Comment on the morphology of the erythrocytes.
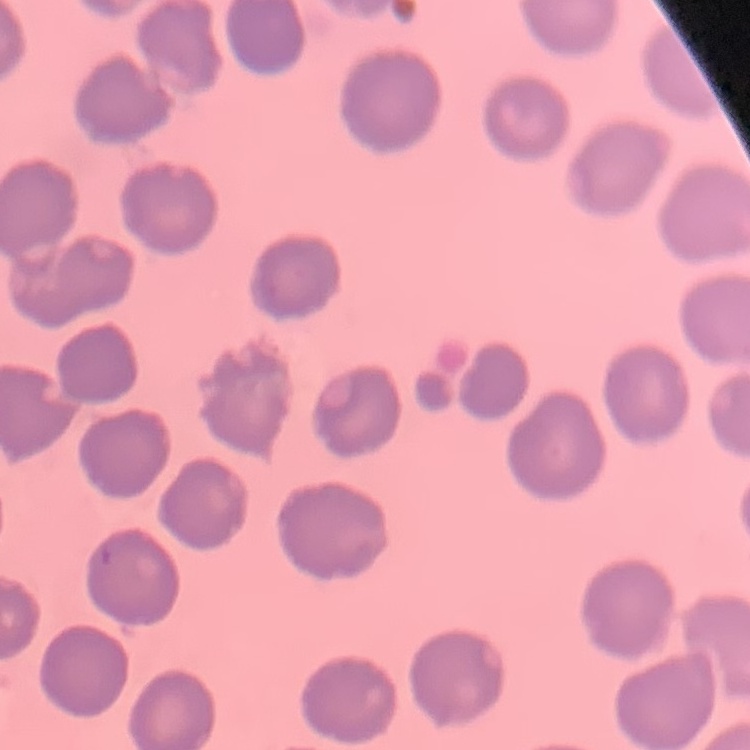

They show no rouleaux formation.

Summary:
  - Preparation: thin peripheral smear
  - Image type: square crop of a larger photomicrograph
  - Stain: Field's or Giemsa